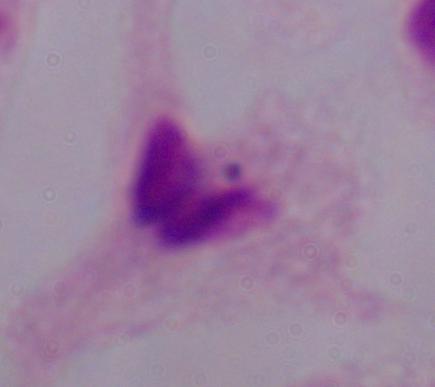

Photomicrograph. 1000x magnification. A trichomonad is seen.